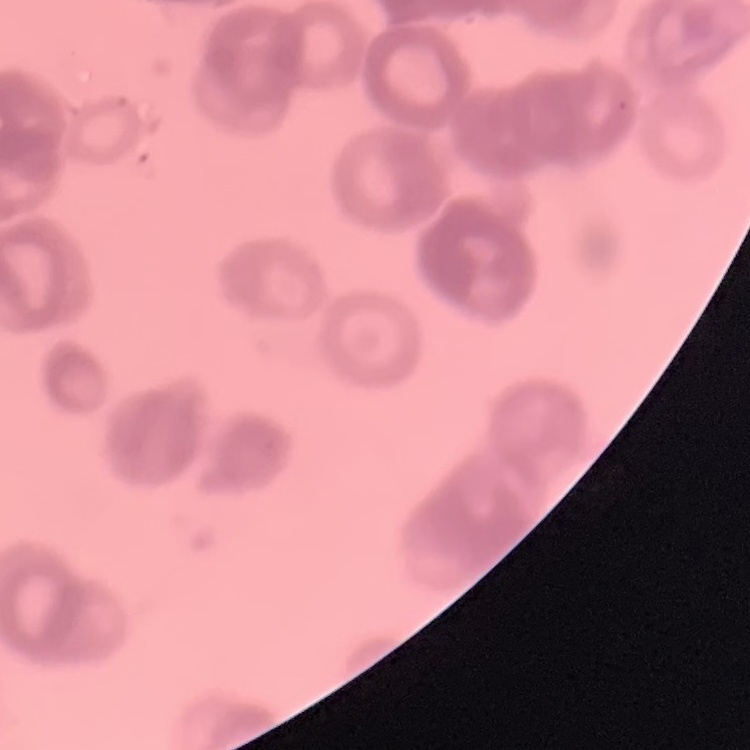
{
  "red_blood_cell_morphology": "rouleaux formation",
  "stain": "Field's or Giemsa",
  "preparation": "thin peripheral smear",
  "image_type": "one tile cut from a larger photomicrograph"
}